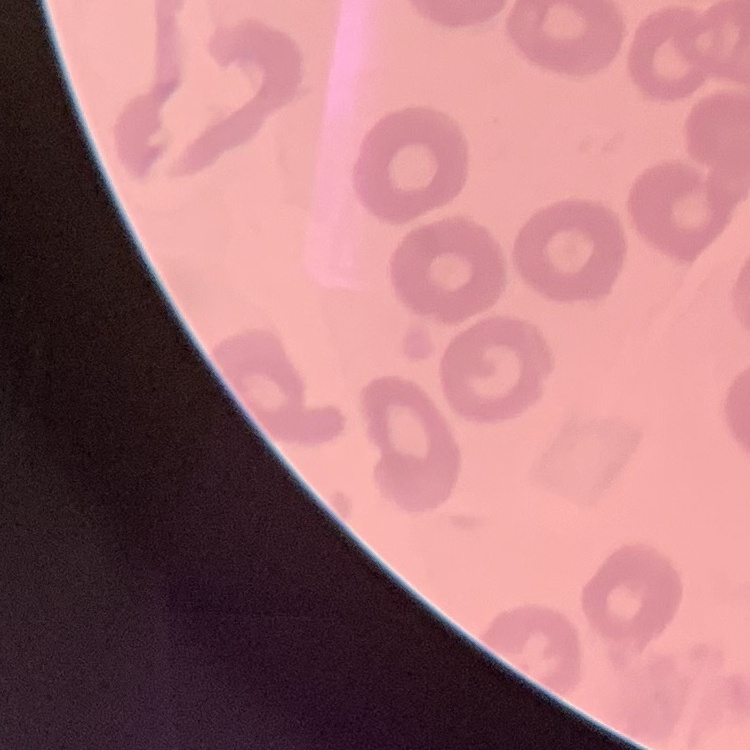 The red blood cells exhibit no rouleaux formation. Stained with either Field's or Giemsa. Thin blood smear. One tile cut from a larger photomicrograph.